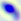

Toxoplasma gondii is shown. Captured at 400x magnification. Photomicrograph.